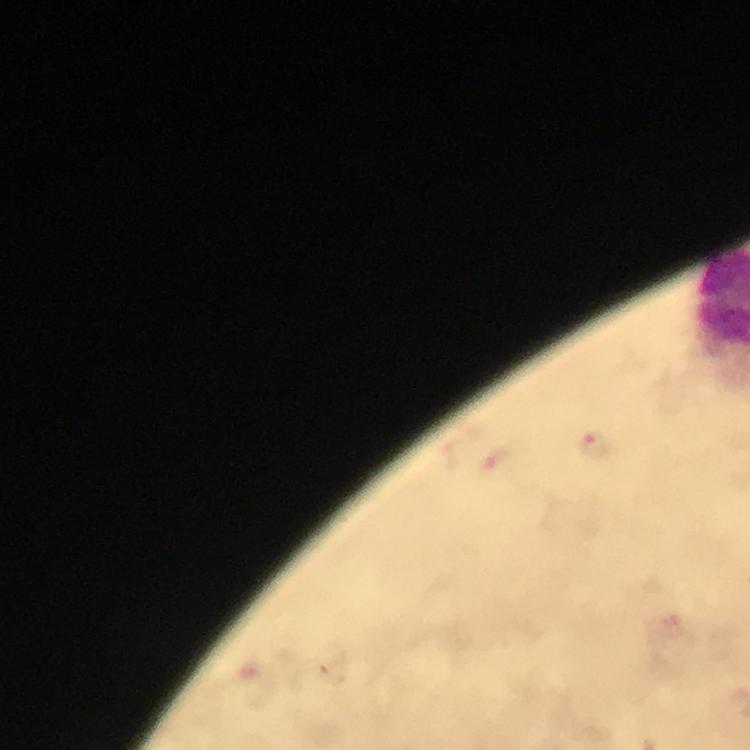

Approximate object centers, in pixels from the top-left corner.
Summary:
  - Plasmodium parasite locations: (x=593, y=444)
  - Preparation: thick blood film
  - Context: from a malaria diagnostic workup
  - Capture: smartphone camera through the microscope
  - Image size: 750×750 pixels
  - Stain: Giemsa
  - Immersion oil: used
  - Magnification: 100x
  - Cropped from: a single field of view